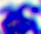

Summary:
  - Modality: photomicrograph
  - Identification: leukocyte
  - Magnification: 400x